Name the cell type shown.
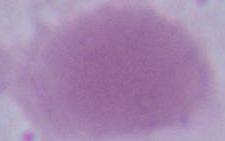
An erythrocyte.

Micrograph. Captured at 1000x magnification.